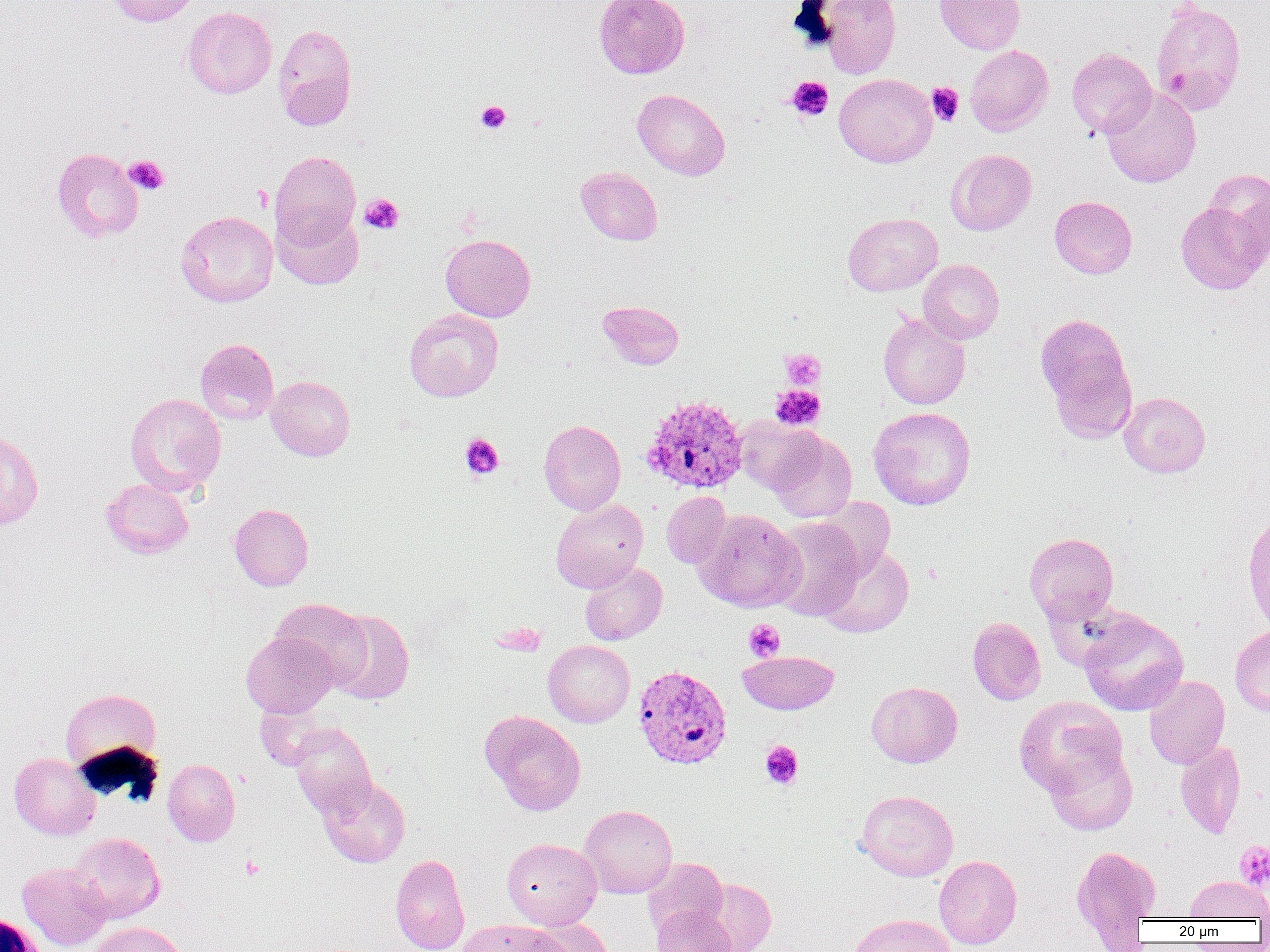
slide_level_diagnosis: Plasmodium vivax
preparation: thin blood smear
platelet_locations: 'approximate bounding boxes as named x1/y1/x2/y2 corners in pixels: (x1=1166, y1=70, x2=1192, y2=92), (x1=786, y1=76, x2=834, y2=121), (x1=927, y1=82, x2=964, y2=126), (x1=475, y1=100, x2=511, y2=133), (x1=124, y1=155, x2=169, y2=195), (x1=252, y1=184, x2=273, y2=212), (x1=359, y1=193, x2=404, y2=235), (x1=780, y1=348, x2=825, y2=389), (x1=770, y1=385, x2=825, y2=430), (x1=460, y1=433, x2=504, y2=479), (x1=744, y1=619, x2=786, y2=662), (x1=760, y1=740, x2=803, y2=790), (x1=1234, y1=840, x2=1270, y2=892), (x1=241, y1=855, x2=264, y2=880)'
field_of_view: one of a larger specimen
white_blood_cell_locations: 'approximate bounding boxes as named x1/y1/x2/y2 corners in pixels: (x1=1, y1=912, x2=48, y2=952)'
image_size: 1270×952 pixels
modality: optical microscopy
uninfected_red_blood_cell_locations: 'approximate bounding boxes as named x1/y1/x2/y2 corners in pixels: (x1=105, y1=0, x2=200, y2=27), (x1=594, y1=0, x2=690, y2=79), (x1=816, y1=0, x2=901, y2=78), (x1=934, y1=0, x2=1025, y2=54), (x1=1150, y1=1, x2=1247, y2=117), (x1=182, y1=6, x2=277, y2=99), (x1=272, y1=24, x2=357, y2=130), (x1=965, y1=45, x2=1053, y2=135), (x1=1066, y1=48, x2=1156, y2=138), (x1=834, y1=74, x2=937, y2=167), (x1=1101, y1=87, x2=1201, y2=188), (x1=632, y1=89, x2=730, y2=180), (x1=51, y1=147, x2=144, y2=242), (x1=946, y1=149, x2=1037, y2=235), (x1=270, y1=150, x2=361, y2=248), (x1=576, y1=167, x2=663, y2=245), (x1=1204, y1=169, x2=1270, y2=260), (x1=1049, y1=195, x2=1137, y2=278), (x1=1175, y1=201, x2=1268, y2=294), (x1=273, y1=207, x2=363, y2=289), (x1=176, y1=211, x2=278, y2=307), (x1=842, y1=212, x2=943, y2=296), (x1=440, y1=234, x2=535, y2=321), (x1=918, y1=259, x2=1004, y2=344), (x1=597, y1=300, x2=685, y2=370), (x1=404, y1=308, x2=504, y2=402), (x1=878, y1=313, x2=970, y2=409), (x1=1035, y1=313, x2=1136, y2=429), (x1=195, y1=338, x2=279, y2=425), (x1=266, y1=375, x2=355, y2=461), (x1=1118, y1=391, x2=1210, y2=477), (x1=125, y1=392, x2=227, y2=496), (x1=868, y1=407, x2=976, y2=510), (x1=736, y1=416, x2=824, y2=494), (x1=539, y1=420, x2=626, y2=515), (x1=0, y1=429, x2=44, y2=531), (x1=768, y1=432, x2=857, y2=523), (x1=100, y1=478, x2=194, y2=558), (x1=662, y1=492, x2=731, y2=568), (x1=810, y1=497, x2=896, y2=578), (x1=551, y1=498, x2=649, y2=593), (x1=229, y1=503, x2=314, y2=592), (x1=692, y1=509, x2=804, y2=612), (x1=1241, y1=509, x2=1270, y2=636), (x1=769, y1=517, x2=865, y2=620), (x1=1024, y1=532, x2=1119, y2=624), (x1=817, y1=545, x2=914, y2=637), (x1=580, y1=562, x2=667, y2=645), (x1=272, y1=598, x2=371, y2=687), (x1=326, y1=609, x2=415, y2=704), (x1=1079, y1=610, x2=1188, y2=716), (x1=968, y1=617, x2=1046, y2=705), (x1=1230, y1=625, x2=1270, y2=716), (x1=241, y1=631, x2=337, y2=718), (x1=543, y1=640, x2=634, y2=727), (x1=738, y1=650, x2=839, y2=714), (x1=1144, y1=675, x2=1229, y2=769), (x1=866, y1=681, x2=962, y2=768), (x1=60, y1=688, x2=162, y2=773), (x1=1015, y1=696, x2=1127, y2=799), (x1=480, y1=710, x2=586, y2=815), (x1=289, y1=723, x2=377, y2=817), (x1=1175, y1=740, x2=1246, y2=838), (x1=1045, y1=745, x2=1138, y2=835), (x1=9, y1=753, x2=100, y2=840), (x1=163, y1=759, x2=240, y2=846), (x1=318, y1=776, x2=410, y2=868), (x1=856, y1=789, x2=959, y2=881), (x1=580, y1=804, x2=677, y2=898), (x1=69, y1=832, x2=165, y2=923), (x1=502, y1=838, x2=602, y2=929), (x1=1071, y1=845, x2=1161, y2=935), (x1=390, y1=854, x2=470, y2=952), (x1=934, y1=855, x2=1022, y2=949), (x1=642, y1=858, x2=728, y2=937), (x1=17, y1=862, x2=112, y2=950), (x1=1185, y1=876, x2=1270, y2=921), (x1=698, y1=879, x2=776, y2=952), (x1=652, y1=905, x2=736, y2=952), (x1=848, y1=913, x2=956, y2=952), (x1=527, y1=918, x2=615, y2=952), (x1=458, y1=919, x2=564, y2=952), (x1=89, y1=922, x2=187, y2=952)'
magnification: 1000x
plasmodium_vivax_infected_red_blood_cell_locations: 'approximate bounding boxes as named x1/y1/x2/y2 corners in pixels: (x1=639, y1=393, x2=748, y2=495), (x1=633, y1=665, x2=732, y2=769)'